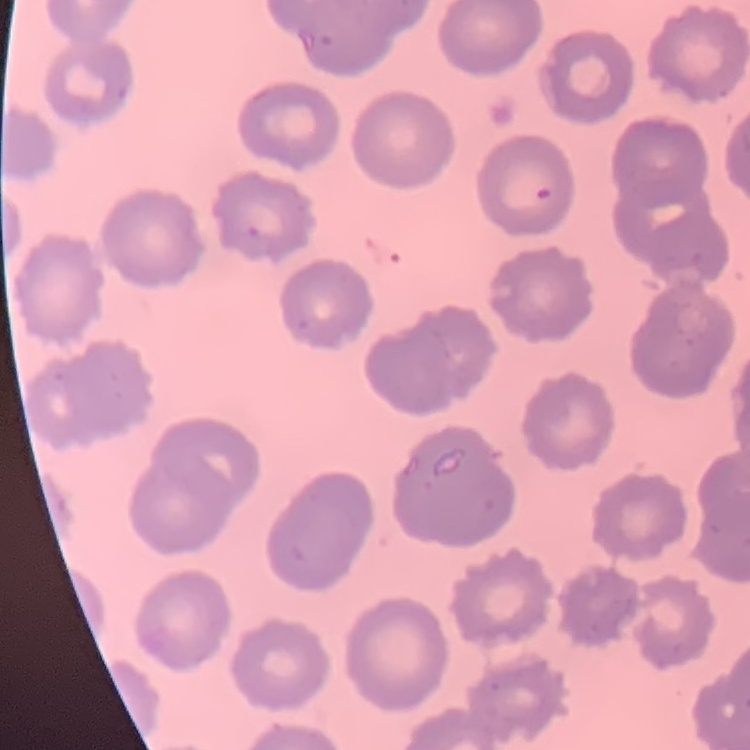

The erythrocytes show no rouleaux formation. Field's or Giemsa stain. One tile cut from a larger photomicrograph. Thin peripheral smear.